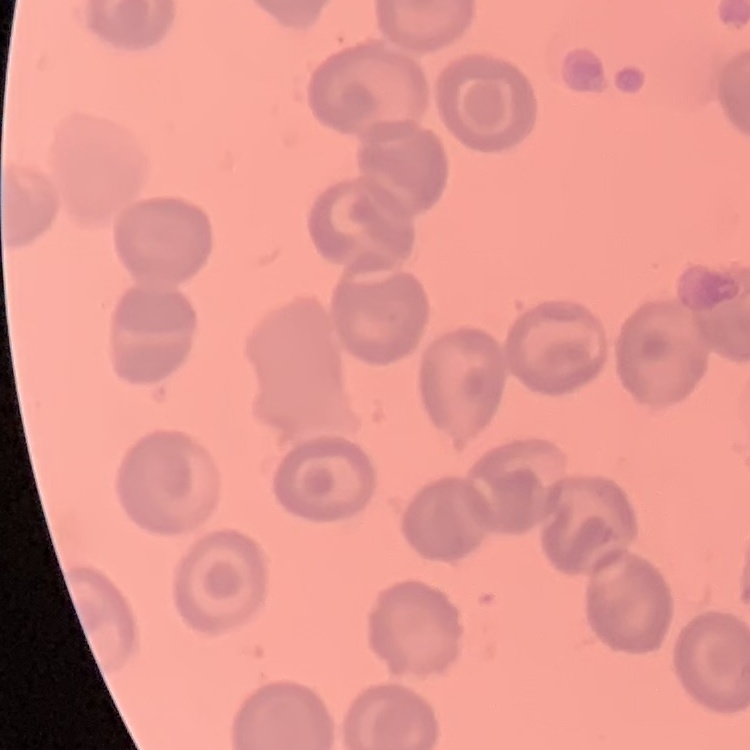
Summary:
  - Red blood cell morphology: no rouleaux formation
  - Image type: square crop of a larger photomicrograph
  - Preparation: thin peripheral smear
  - Stain: Field's or Giemsa